State the blood parasite species.
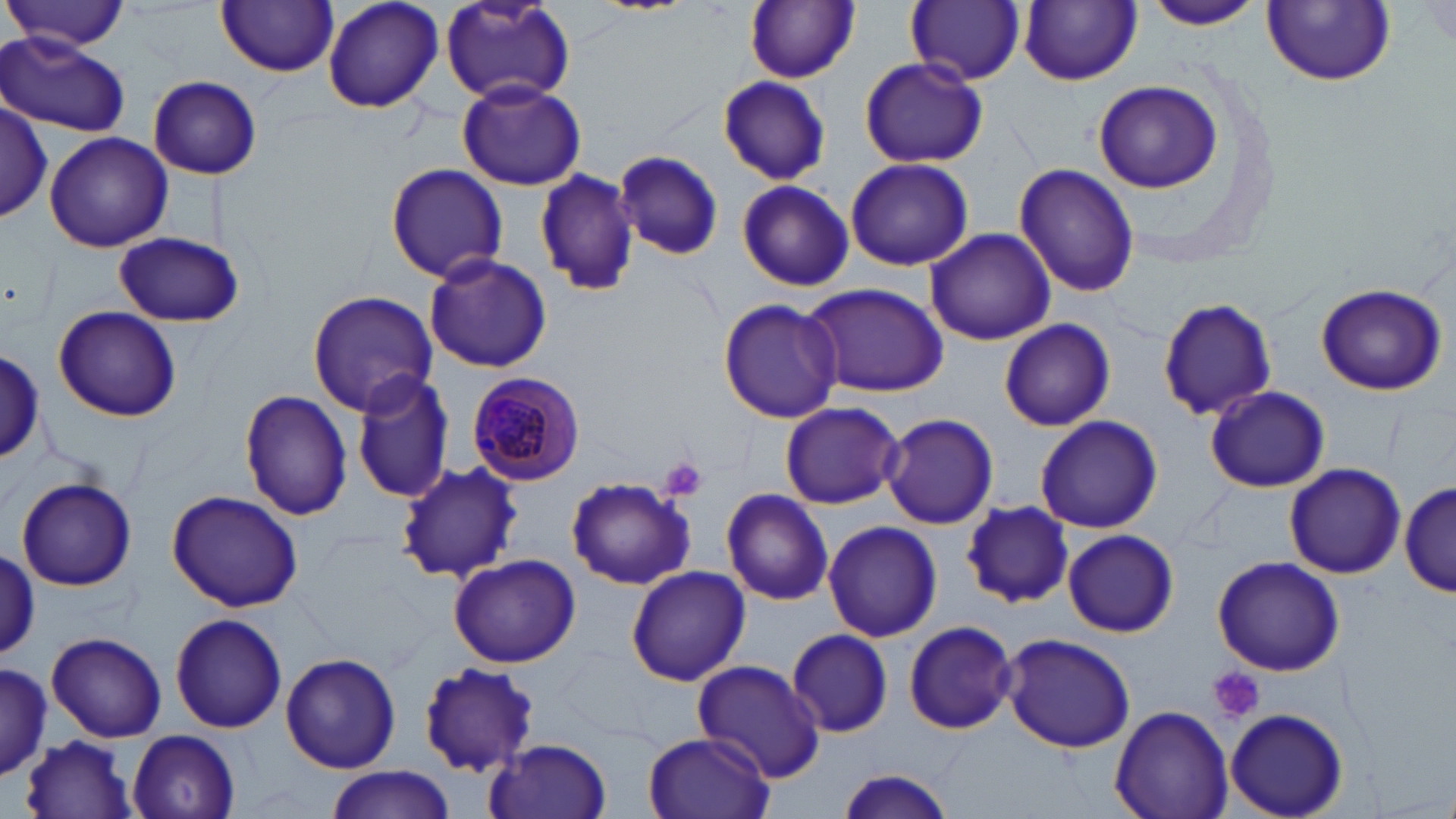

Plasmodium malariae.

preparation = thin blood smear
stain = May-Grünwald-Giemsa
uninfected red blood cell locations = approximate bounding boxes as (x1,y1)-(x2,y2) corner pairs in pixels: (4,0)-(130,52), (322,0)-(445,115), (588,0)-(699,15), (744,0)-(860,84), (907,0)-(1026,87), (1137,0)-(1271,31), (218,1)-(339,76), (439,1)-(576,108), (1264,1)-(1395,87), (1020,2)-(1140,86), (1417,3)-(1456,50), (0,34)-(128,137), (858,59)-(987,168), (715,74)-(831,185), (149,75)-(264,180), (457,79)-(586,192), (1093,79)-(1224,192), (0,99)-(52,220), (44,131)-(171,253), (616,149)-(724,261), (845,157)-(973,272), (384,162)-(509,282), (1014,163)-(1138,297), (535,168)-(642,296), (736,179)-(854,293), (925,228)-(1057,346), (113,230)-(245,327), (423,252)-(552,373), (799,282)-(950,397), (1316,283)-(1447,395), (306,289)-(440,415), (1158,295)-(1278,422), (717,297)-(845,424), (52,306)-(182,423), (996,318)-(1116,430), (0,349)-(44,467), (350,371)-(456,504), (1206,385)-(1329,492), (239,389)-(354,522), (778,401)-(905,510), (880,412)-(999,531), (1034,415)-(1163,533), (397,461)-(521,583), (1283,463)-(1406,578), (565,475)-(696,591), (16,477)-(138,591), (1401,480)-(1453,598), (721,487)-(834,605), (166,489)-(304,611), (959,501)-(1073,607), (823,521)-(943,643), (1062,528)-(1178,637), (1,545)-(41,661), (448,552)-(582,668), (1213,556)-(1345,676), (625,565)-(750,686), (169,613)-(288,733), (902,619)-(1019,734), (787,628)-(893,738), (47,632)-(167,743), (1000,632)-(1137,753), (279,651)-(401,774), (691,660)-(827,783), (0,661)-(52,778), (417,661)-(540,773), (1110,705)-(1232,819), (1224,708)-(1347,818), (128,729)-(238,819), (642,731)-(773,819), (20,734)-(138,819), (485,738)-(613,819), (325,765)-(452,819), (832,767)-(958,819)
image size = 1456×819 pixels
magnification = 1000x
platelet locations = approximate bounding boxes as (x1,y1)-(x2,y2) corner pairs in pixels: (659,456)-(708,502), (1210,667)-(1264,723)
modality = light microscopy
field of view = single
Plasmodium malariae-infected red blood cell locations = approximate bounding boxes as (x1,y1)-(x2,y2) corner pairs in pixels: (467,372)-(587,484)